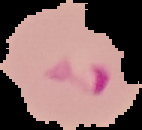
image_size: 142×130 pixels
image_type: segmented cell region with the area outside set to black
preparation: thin blood film
malaria_status: parasitized